Locate and identify every blood parasite.
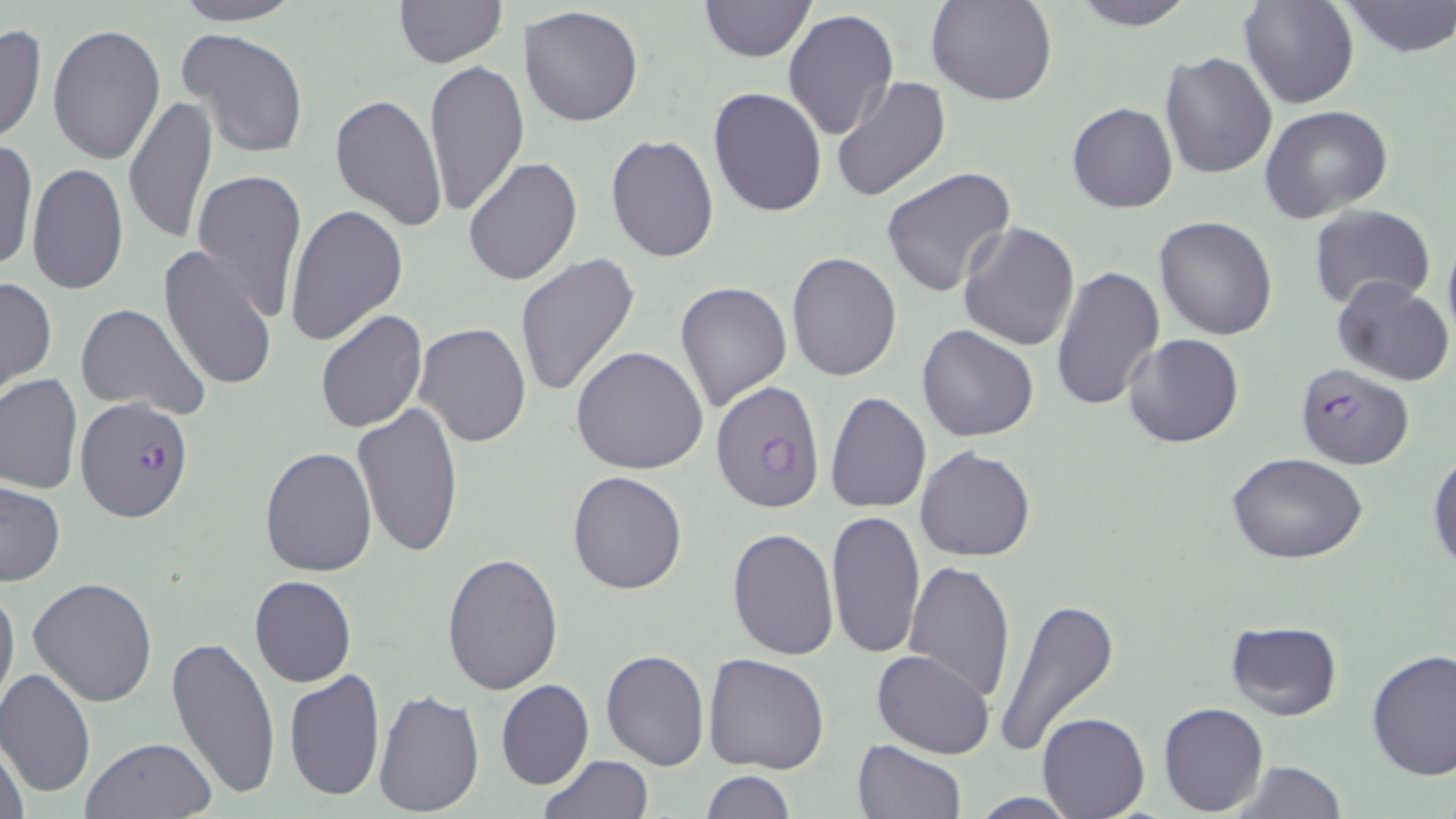

Approximate bounding boxes as (x1, y1, x2, y2) in pixels.
Plasmodium falciparum-infected red blood cells: (1295, 364, 1414, 470), (711, 380, 827, 512), (75, 396, 193, 522).
No Plasmodium ovale, Plasmodium malariae, Plasmodium vivax, Babesia divergens, or Trypanosoma brucei observed.

slide-level diagnosis = Plasmodium falciparum
image size = 1456×819 pixels
field of view = one of a larger specimen
stain = May-Grünwald-Giemsa
modality = optical microscopy
magnification = 1000x
uninfected red blood cell locations = approximate bounding boxes as (x1, y1, x2, y2) in pixels: (167, 0, 306, 25), (699, 0, 816, 63), (928, 0, 1057, 106), (1069, 0, 1197, 30), (1340, 0, 1454, 58), (392, 1, 508, 68), (1238, 1, 1358, 108), (518, 5, 644, 127), (784, 9, 899, 142), (47, 21, 164, 165), (0, 23, 49, 146), (179, 28, 310, 160), (1159, 53, 1277, 179), (424, 58, 529, 218), (831, 77, 951, 204), (708, 86, 827, 217), (330, 94, 448, 228), (124, 96, 218, 247), (1068, 103, 1178, 214), (1262, 106, 1392, 225), (606, 134, 719, 262), (1, 138, 36, 272), (464, 156, 581, 287), (27, 163, 128, 295), (880, 167, 1021, 301), (191, 168, 308, 320), (284, 204, 408, 346), (1308, 204, 1434, 311), (1153, 216, 1278, 339), (958, 221, 1080, 351), (1442, 228, 1456, 347), (159, 244, 280, 395), (787, 252, 901, 380), (514, 253, 640, 399), (1051, 265, 1165, 410), (0, 274, 57, 396), (1332, 278, 1454, 385), (676, 279, 793, 413), (75, 303, 208, 420), (316, 309, 428, 432), (413, 323, 531, 449), (916, 325, 1039, 442), (1124, 334, 1244, 449), (571, 346, 708, 474), (0, 374, 83, 494), (825, 391, 931, 513), (353, 401, 463, 557), (259, 446, 377, 577), (916, 446, 1036, 562), (1428, 451, 1456, 572), (1226, 454, 1368, 563), (568, 471, 686, 593), (0, 481, 66, 588), (825, 510, 926, 657), (727, 528, 838, 659), (442, 549, 564, 695), (904, 560, 1017, 701), (249, 575, 357, 688), (29, 577, 159, 706), (0, 580, 19, 713), (993, 594, 1119, 760), (1224, 619, 1343, 720), (166, 633, 282, 801), (602, 648, 710, 769), (1365, 648, 1455, 780), (872, 649, 994, 759), (702, 652, 831, 774), (0, 667, 95, 798), (285, 667, 385, 802), (496, 679, 595, 790), (374, 688, 485, 813), (1159, 703, 1268, 815), (1038, 712, 1149, 818), (80, 735, 219, 819), (1, 737, 30, 819), (851, 740, 966, 819), (537, 754, 654, 818), (1232, 759, 1346, 819), (701, 771, 796, 817), (965, 793, 1087, 818)
preparation = thin blood film